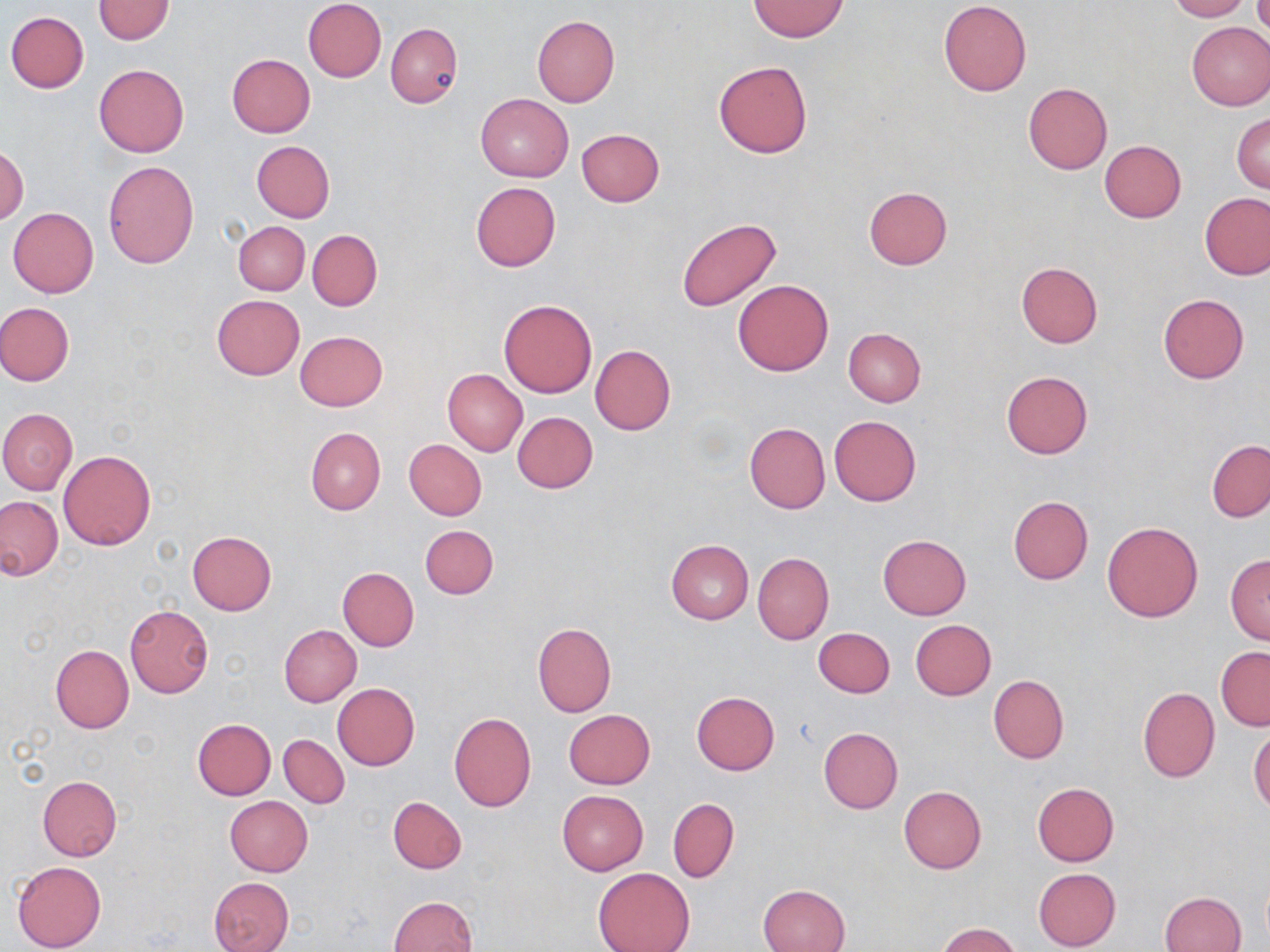

{
  "slide_level_diagnosis": "no evidence of blood parasites",
  "magnification": "1000x",
  "modality": "light microscopy",
  "image_size": "1270×952 pixels",
  "field_of_view": "single",
  "preparation": "thin blood film",
  "stain": "May-Grünwald-Giemsa",
  "uninfected_red_blood_cell_locations": "approximate bounding boxes as (x1,y1)-(x2,y2) corner pairs in pixels: (303,0)-(386,82), (1167,0)-(1252,22), (92,1)-(174,44), (749,1)-(849,41), (938,1)-(1031,95), (6,11)-(88,93), (532,15)-(620,106), (385,22)-(463,107), (1186,22)-(1270,111), (227,54)-(315,136), (714,60)-(812,158), (94,64)-(189,157), (1023,82)-(1112,175), (477,93)-(573,183), (1232,113)-(1270,193), (576,128)-(665,206), (1098,140)-(1187,223), (251,141)-(334,222), (0,144)-(28,225), (103,161)-(199,269), (471,182)-(560,271), (863,186)-(952,269), (1201,192)-(1270,279), (7,208)-(98,298), (674,217)-(783,314), (234,221)-(310,295), (308,230)-(381,311), (1016,261)-(1103,347), (733,279)-(833,377), (1158,294)-(1248,383), (212,296)-(303,379), (498,299)-(598,398), (0,303)-(74,385), (844,329)-(925,407), (295,330)-(387,411), (590,345)-(675,435), (442,369)-(527,456), (1001,371)-(1094,459), (0,408)-(77,494), (511,411)-(598,493), (829,415)-(921,506), (744,422)-(830,514), (305,428)-(385,515), (404,438)-(487,521), (1207,439)-(1270,522), (59,450)-(155,550), (0,496)-(63,580), (1009,496)-(1093,584), (1102,521)-(1203,623), (420,524)-(499,599), (187,531)-(276,616), (878,534)-(971,620), (666,540)-(753,625), (752,553)-(834,644), (1226,554)-(1270,644), (337,567)-(419,651), (124,605)-(214,698), (910,620)-(997,700), (533,622)-(616,716), (280,625)-(361,706), (813,627)-(895,698), (50,645)-(133,733), (1216,646)-(1270,730), (988,674)-(1068,764), (332,683)-(420,770), (1138,687)-(1220,782), (691,691)-(779,776), (563,709)-(655,789), (449,712)-(536,811), (193,719)-(275,799), (818,727)-(903,813), (1248,727)-(1270,814), (279,735)-(349,808), (37,776)-(122,861), (1032,782)-(1119,866), (899,786)-(986,874), (557,790)-(648,875), (225,796)-(313,876), (388,796)-(466,874), (668,797)-(739,883), (12,860)-(106,952), (593,867)-(695,952), (1033,868)-(1121,951), (208,877)-(294,952), (758,884)-(850,952), (1159,891)-(1247,952), (388,896)-(478,952), (938,922)-(1023,952)"
}